Point out each Plasmodium parasite.
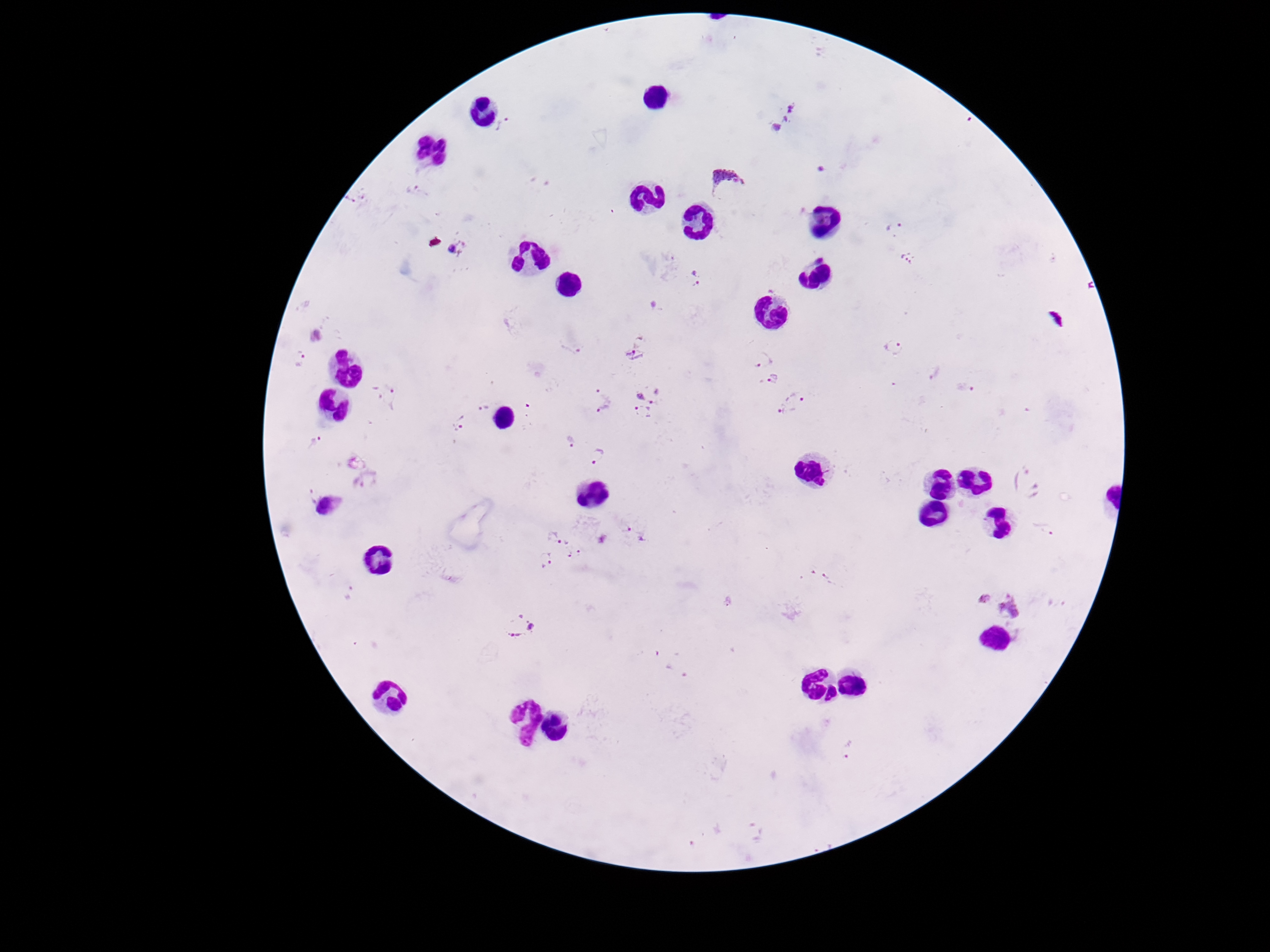

Approximate centers as {x, y} in pixels.
Plasmodium parasites: {782, 116}, {505, 125}, {821, 168}, {723, 177}, {415, 191}, {359, 198}, {895, 229}, {460, 246}, {909, 258}, {695, 277}, {316, 336}, {576, 347}, {634, 348}, {893, 348}, {300, 357}, {764, 359}, {934, 374}, {773, 380}, {651, 389}, {966, 389}, {603, 392}, {801, 393}, {392, 397}, {483, 407}, {606, 409}, {785, 409}, {643, 413}, {459, 424}, {317, 440}, {571, 441}, {597, 456}, {313, 495}, {330, 509}, {1044, 528}, {627, 529}, {553, 537}, {573, 549}, {545, 559}, {821, 577}, {728, 600}, {1001, 600}, {520, 625}, {848, 749}.

Summary:
  - Patient malaria status: infected
  - Image size: 1270×952 pixels
  - Preparation: thick blood film
  - Magnification: 100x
  - Capture: smartphone camera through the microscope eyepiece
  - Stain: Giemsa
  - Field of view: single